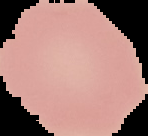

Summary:
  - Image size: 148×136 pixels
  - Image type: segmented cell region on a black background
  - Preparation: thin blood smear
  - Result: no malaria parasites detected